Assess this cell for malaria.
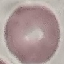
It is uninfected.

preparation = thin smear
stain = Giemsa
capture = smartphone camera at the microscope eyepiece
image type = automatically extracted cell patch, resized to 64 × 64 pixels